State which parasite is depicted.
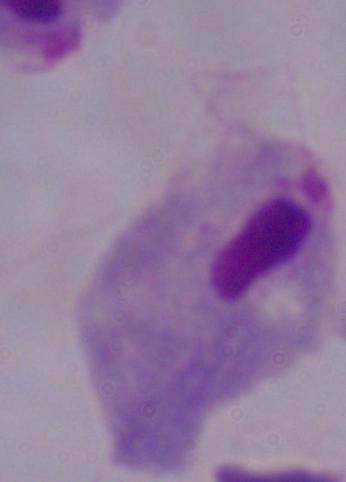
This is a trichomonad.

Micrograph. Captured at 1000x magnification.